Give the extent of all Plasmodium falciparum-infected red blood cells.
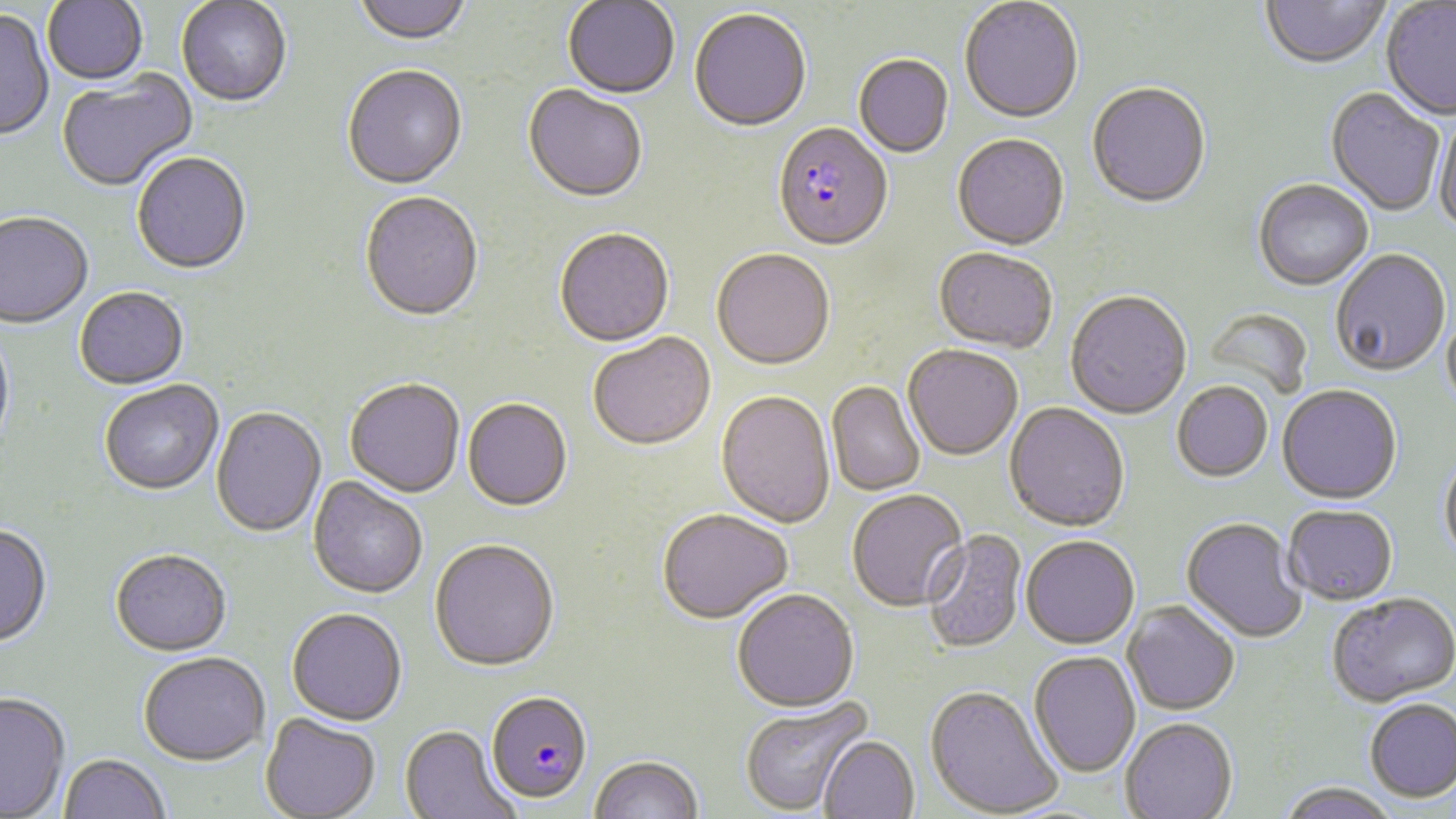
Approximate bounding boxes as (x1, y1, x2, y2) in pixels.
Plasmodium falciparum-infected red blood cells: (772, 125, 893, 254), (486, 691, 592, 804).

Uninfected red blood cell locations: (43, 0, 147, 86), (353, 0, 473, 48), (177, 1, 292, 109), (563, 1, 679, 101), (959, 1, 1084, 126), (1260, 1, 1389, 72), (1381, 2, 1456, 121), (0, 10, 54, 142), (689, 10, 812, 134), (854, 56, 954, 159), (342, 67, 468, 191), (57, 71, 198, 193), (1087, 85, 1211, 212), (522, 86, 648, 204), (1325, 89, 1444, 218), (1433, 116, 1456, 237), (952, 136, 1069, 253), (132, 153, 252, 275), (1253, 181, 1373, 292), (360, 193, 484, 323), (0, 214, 93, 330), (554, 229, 675, 349), (933, 249, 1057, 355), (711, 250, 835, 372), (1330, 251, 1451, 378), (75, 289, 189, 390), (1065, 292, 1192, 421), (1203, 308, 1314, 400), (1442, 308, 1456, 413), (0, 327, 15, 458), (588, 332, 716, 451), (903, 345, 1023, 462), (344, 379, 465, 498), (99, 381, 224, 495), (826, 381, 925, 496), (1172, 382, 1273, 482), (1277, 386, 1402, 506), (716, 391, 836, 529), (463, 399, 572, 512), (1004, 402, 1130, 533), (211, 407, 326, 538), (1439, 453, 1456, 571), (308, 476, 428, 598), (847, 489, 968, 612), (1283, 505, 1398, 606), (657, 509, 792, 625), (1181, 517, 1307, 645), (0, 525, 53, 648), (921, 530, 1027, 654), (1020, 536, 1139, 650), (429, 540, 559, 673), (111, 548, 232, 656), (732, 589, 859, 713), (1327, 594, 1456, 708), (1122, 601, 1239, 716), (286, 607, 407, 726), (139, 651, 270, 765), (1029, 651, 1141, 778), (925, 686, 1063, 817), (0, 692, 70, 818), (739, 697, 873, 815), (1364, 699, 1456, 803), (259, 713, 381, 819), (1120, 718, 1238, 819), (399, 724, 519, 819), (818, 735, 919, 818), (58, 753, 171, 819), (589, 755, 705, 819), (1275, 784, 1401, 819). Slide-level diagnosis: Plasmodium falciparum. Thin blood smear. Optical microscopy. Captured at 1000x magnification. Image is 1456×819 pixels. One field of a larger specimen. May-Grünwald-Giemsa-stained preparation.